Give the extent of all uninfected red blood cells.
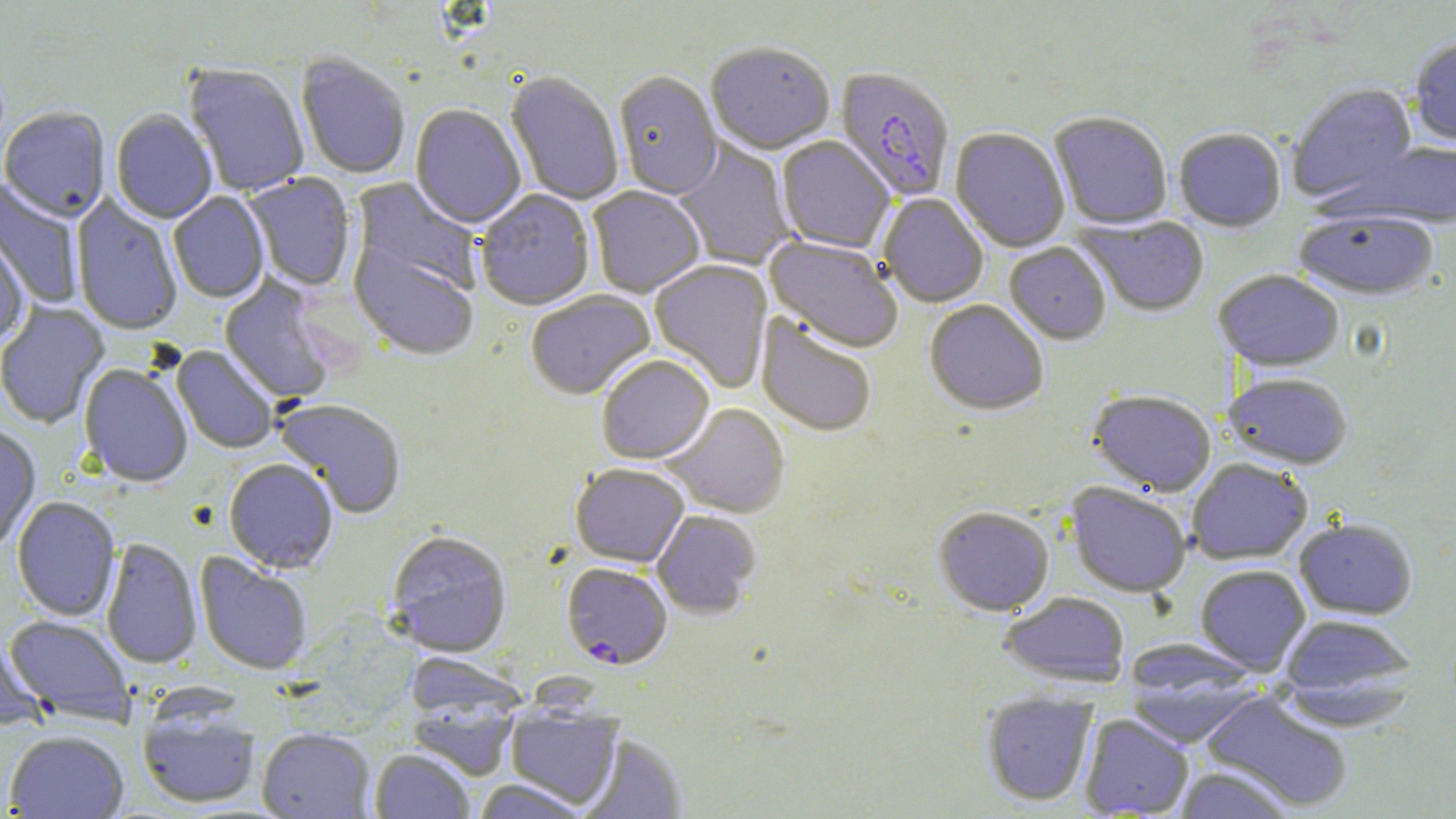
Approximate bounding boxes as [x1, y1, x2, y2] in pixels.
Uninfected red blood cells: [1409, 39, 1456, 147], [705, 45, 835, 158], [296, 56, 410, 180], [183, 65, 309, 198], [505, 74, 624, 206], [613, 74, 723, 201], [1288, 84, 1418, 205], [409, 105, 526, 230], [0, 109, 111, 223], [111, 110, 217, 224], [1049, 113, 1173, 232], [950, 129, 1070, 253], [1174, 130, 1286, 233], [776, 137, 894, 255], [673, 139, 797, 271], [1351, 140, 1456, 228], [242, 174, 357, 292], [0, 178, 85, 309], [349, 178, 483, 301], [587, 186, 705, 298], [476, 190, 596, 313], [168, 192, 270, 304], [71, 194, 183, 337], [879, 194, 988, 308], [1293, 213, 1438, 302], [1074, 215, 1211, 317], [0, 227, 30, 350], [348, 237, 480, 363], [764, 237, 904, 354], [1004, 243, 1111, 346], [649, 259, 774, 393], [1213, 270, 1344, 373], [219, 274, 338, 406], [525, 291, 656, 402], [0, 301, 110, 429], [924, 301, 1048, 417], [756, 313, 877, 437], [171, 345, 279, 454], [596, 357, 715, 465], [79, 365, 193, 489], [1222, 373, 1354, 470], [1087, 390, 1216, 498], [274, 400, 407, 519], [662, 403, 791, 518], [0, 425, 41, 553], [1187, 458, 1312, 565], [223, 460, 338, 575], [570, 465, 689, 569], [1065, 483, 1191, 598], [11, 497, 121, 623], [933, 507, 1054, 617], [652, 511, 761, 620], [1294, 518, 1418, 620], [385, 532, 512, 658], [100, 538, 202, 670], [194, 552, 312, 676], [1195, 565, 1311, 675], [1000, 593, 1130, 688], [3, 616, 135, 727], [1278, 616, 1417, 709], [0, 630, 47, 730], [408, 654, 522, 723], [1122, 655, 1263, 747], [1201, 690, 1353, 813], [981, 691, 1098, 807], [137, 700, 261, 810], [407, 702, 520, 781], [505, 706, 623, 811], [1080, 714, 1194, 818], [257, 729, 375, 819], [4, 731, 129, 818], [581, 735, 686, 818], [369, 749, 474, 819], [1171, 765, 1296, 819], [473, 779, 592, 818].

Summary:
  - Plasmodium falciparum-infected red blood cell locations: [833, 68, 955, 203], [561, 564, 672, 670]
  - Slide-level diagnosis: Plasmodium falciparum
  - Image size: 1456×819 pixels
  - Field of view: single
  - Modality: optical microscopy
  - Magnification: 1000x
  - Preparation: thin blood smear
  - Stain: May-Grünwald-Giemsa